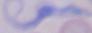 A trypanosome is seen. Captured at 1000x magnification. Micrograph.